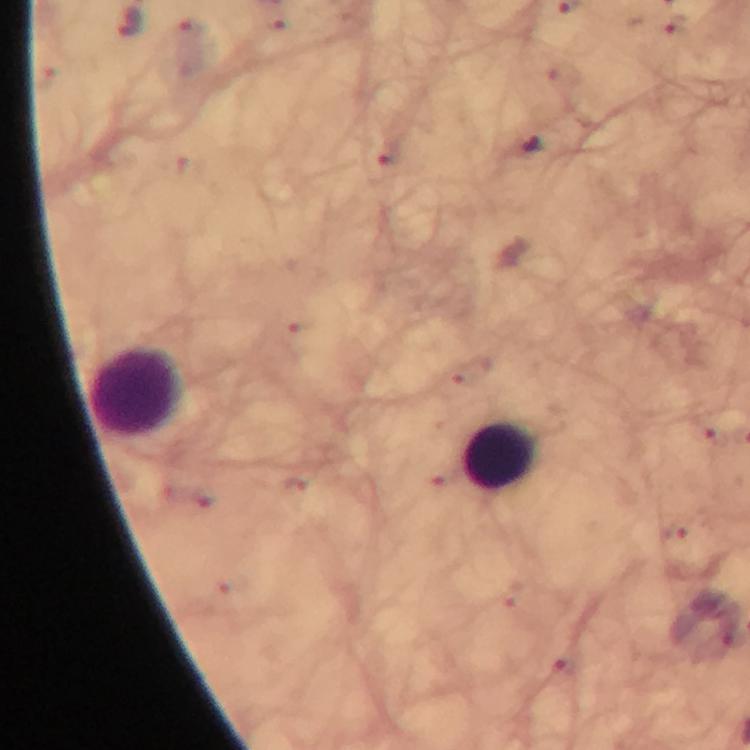

Approximate centers as [x, y] in pixels.
Summary:
  - Plasmodium parasite locations: [532, 146], [674, 532]
  - Leukocyte locations: [137, 393], [501, 457]
  - Context: from a malaria diagnostic workup
  - Cropped from: a single field of view
  - Immersion oil: used
  - Capture: smartphone mounted on the microscope
  - Preparation: thick blood smear
  - Magnification: 100x
  - Image size: 750×750 pixels
  - Stain: Giemsa